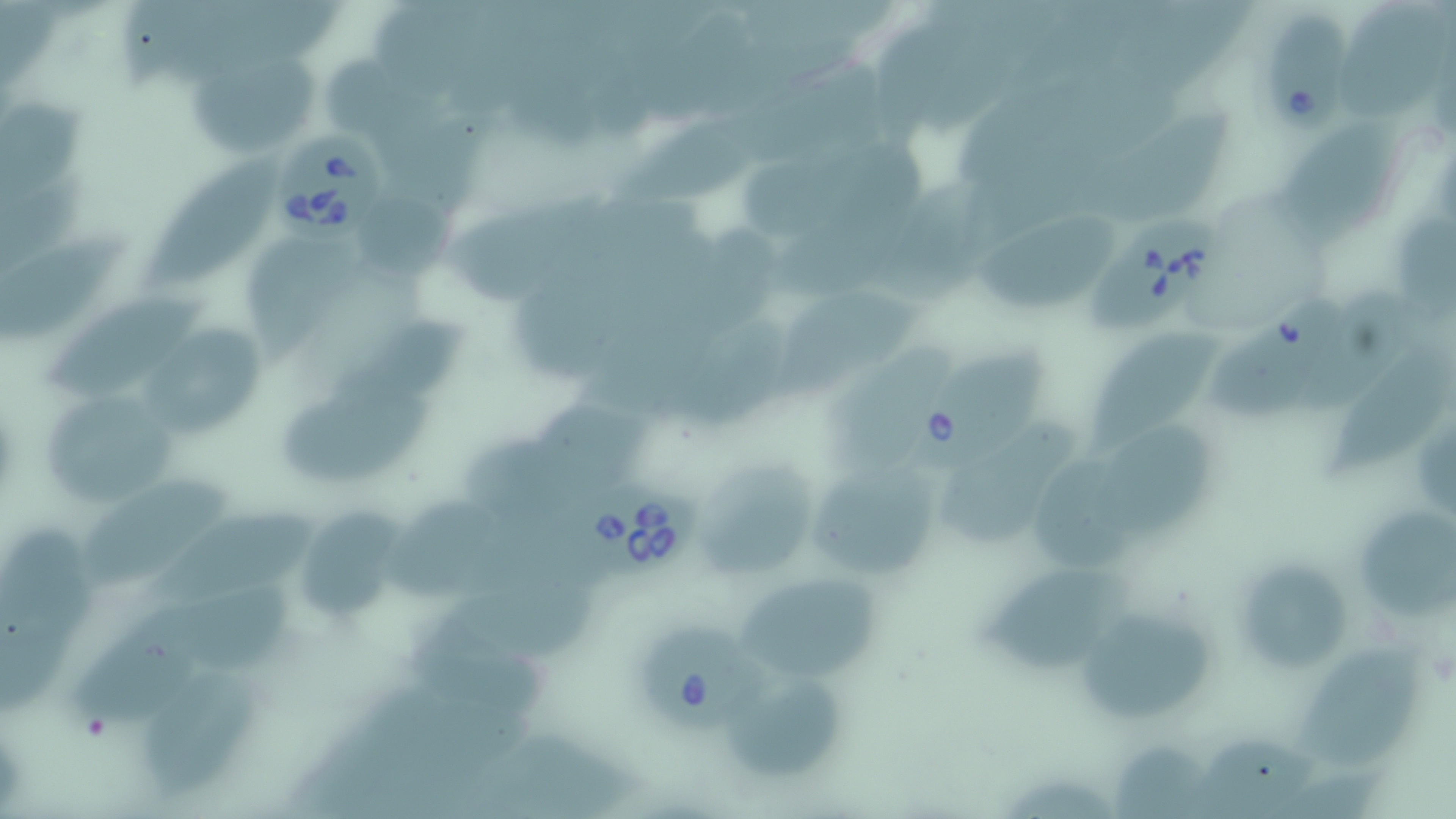
Summary:
  - Coordinate format: approximate bounding boxes as (x1,y1)-(x2,y2) corner pairs in pixels
  - Babesia divergens-infected red blood cell locations: (1262,11)-(1355,134), (274,123)-(388,246), (1086,212)-(1213,336), (914,344)-(1045,469), (575,473)-(695,580), (638,617)-(775,734)
  - Uninfected red blood cell locations: (1337,1)-(1449,120), (645,7)-(757,128), (882,11)-(966,151), (187,48)-(319,160), (325,50)-(472,214), (1031,69)-(1193,179), (1,88)-(92,204), (1090,111)-(1227,227), (621,124)-(745,210), (1278,124)-(1393,240), (775,147)-(923,295), (141,150)-(284,293), (875,175)-(1055,306), (443,192)-(613,307), (360,194)-(452,287), (970,210)-(1121,315), (1399,217)-(1456,317), (689,231)-(779,345), (3,232)-(132,340), (246,236)-(381,362), (503,275)-(627,384), (780,283)-(924,406), (44,287)-(213,399), (1309,288)-(1427,414), (1216,300)-(1341,414), (331,316)-(468,397), (143,320)-(262,444), (1095,322)-(1225,453), (1329,345)-(1455,480), (280,378)-(444,486), (542,385)-(652,493), (39,387)-(181,508), (1090,421)-(1225,542), (468,438)-(599,526), (1032,451)-(1135,584), (693,453)-(822,587), (801,457)-(951,583), (66,475)-(240,590), (392,495)-(499,601), (1359,503)-(1454,621), (301,504)-(405,615), (156,509)-(319,606), (1,521)-(91,643), (477,530)-(595,659), (1241,556)-(1349,671), (982,564)-(1142,673), (748,576)-(885,680), (188,582)-(310,674), (1078,604)-(1218,725), (414,606)-(543,715), (75,610)-(202,731), (1295,643)-(1425,776), (145,669)-(265,799), (737,681)-(850,791), (1181,731)-(1319,819), (475,735)-(642,819), (1116,741)-(1213,819), (1004,771)-(1119,819)
  - Slide-level diagnosis: Babesia divergens
  - Modality: light microscopy
  - Image size: 1456×819 pixels
  - Magnification: 1000x
  - Preparation: thin blood film
  - Stain: May-Grünwald-Giemsa
  - Field of view: one of a larger specimen